Report the malaria status of this cell.
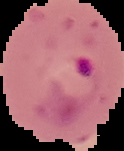

It is parasitized.

Summary:
  - Image size: 124×151 pixels
  - Preparation: thin blood film
  - Image type: cell region segmented out of the field of view; surrounding area masked to black